Classify this cell by malaria status.
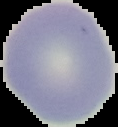

Uninfected.

From a thin blood film. Image is 118×127 pixels. Cell region segmented out of the field of view; the surrounding area is masked to black.